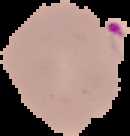
From a thin blood smear. Segmented cell region on a black background. Image is 130×136 pixels. Result: Plasmodium parasites detected.